Identify the cell.
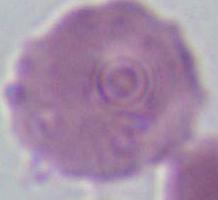

An erythrocyte.

Summary:
  - Magnification: 1000x
  - Modality: micrograph